Name the blood parasite species.
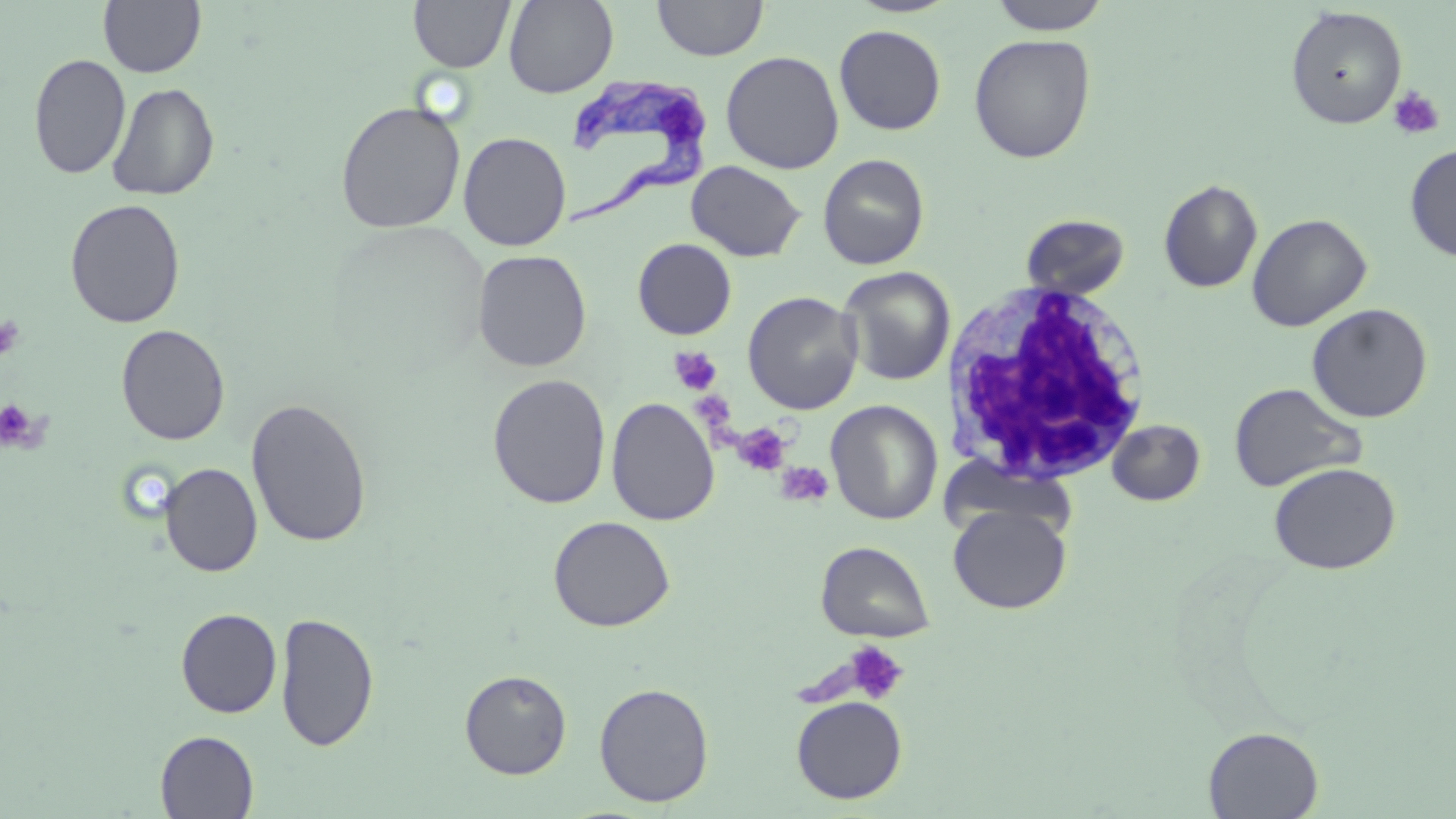

Trypanosoma brucei.

Summary:
  - Coordinate format: approximate bounding boxes as (x1, y1, x2, y2) in pixels
  - Uninfected red blood cell locations: (504, 0, 617, 97), (652, 0, 768, 61), (988, 0, 1113, 35), (98, 1, 206, 78), (409, 1, 515, 72), (1285, 6, 1407, 129), (834, 24, 946, 135), (969, 34, 1096, 163), (720, 50, 844, 174), (28, 53, 131, 180), (107, 82, 219, 201), (335, 101, 466, 234), (458, 132, 571, 251), (1404, 143, 1456, 263), (817, 154, 930, 270), (686, 160, 806, 262), (1158, 179, 1262, 293), (64, 198, 186, 328), (1247, 213, 1372, 331), (1020, 214, 1131, 299), (632, 238, 737, 339), (472, 250, 592, 373), (838, 266, 956, 386), (742, 291, 863, 415), (1306, 303, 1433, 423), (116, 324, 231, 446), (487, 374, 611, 509), (1228, 382, 1367, 492), (245, 396, 373, 548), (606, 397, 720, 525), (826, 400, 943, 524), (1107, 419, 1205, 506), (1269, 462, 1401, 575), (159, 463, 262, 577), (948, 505, 1071, 614), (548, 515, 675, 632), (816, 540, 935, 642), (175, 608, 282, 718), (274, 611, 380, 752), (459, 669, 572, 779), (593, 681, 715, 807), (791, 696, 907, 804), (1203, 726, 1324, 818), (155, 730, 259, 818)
  - White blood cell locations: (941, 282, 1153, 487)
  - Trypanosoma brucei locations: (551, 76, 715, 230)
  - Platelet locations: (1388, 87, 1445, 140), (0, 315, 25, 362), (669, 347, 723, 396), (695, 389, 737, 432), (0, 399, 38, 450), (733, 422, 792, 477), (775, 461, 834, 506), (844, 641, 909, 705)
  - Field of view: single
  - Stain: May-Grünwald-Giemsa
  - Preparation: thin blood smear
  - Modality: light microscopy
  - Image size: 1456×819 pixels
  - Magnification: 1000x